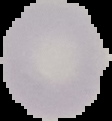

image type = segmented cell region on a black background
preparation = thin blood film
image size = 112×121 pixels
result = no Plasmodium parasites seen